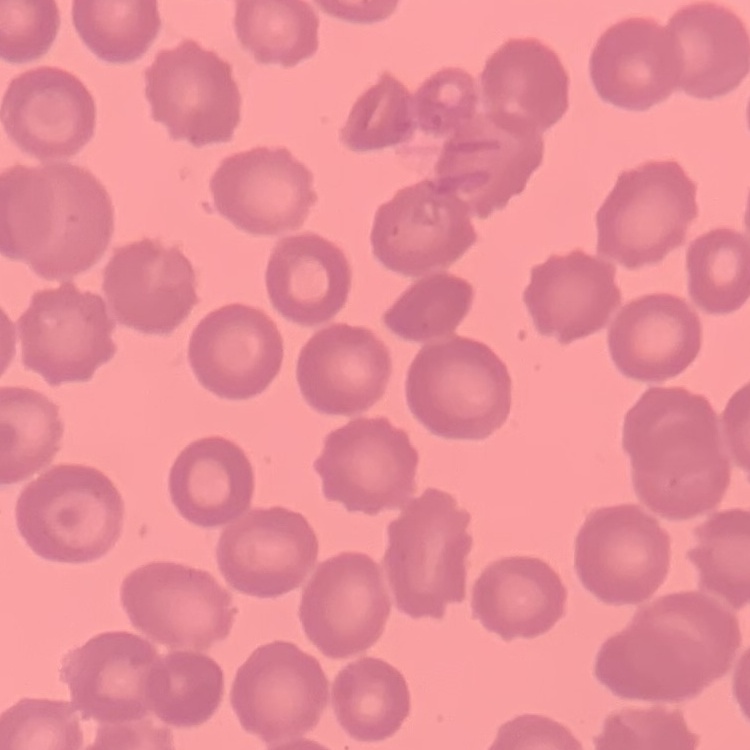
The red blood cells show no rouleaux formation. Thin peripheral smear. Square crop of a larger photomicrograph. Stained with either Field's or Giemsa.